Identify the cell.
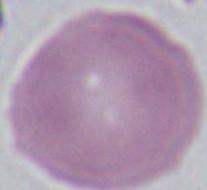
An erythrocyte.

1000x magnification. Photomicrograph.